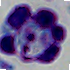

Micrograph. Captured at 1000x magnification. A leukocyte is shown.